State which parasite is depicted.
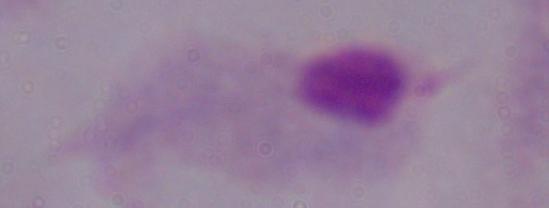

This is a trichomonad.

1000x magnification. Photomicrograph.